Report the malaria status of this cell.
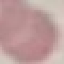

Uninfected.

preparation: thin blood smear
image_type: automatically extracted cell patch, resized to 64 × 64 pixels
capture: smartphone through the microscope eyepiece
stain: Giemsa